Name the cell type shown.
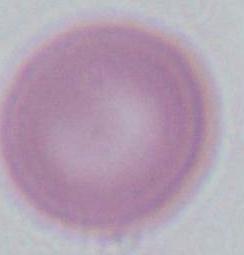
This is an erythrocyte.

{
  "modality": "photomicrograph",
  "magnification": "1000x"
}